Name the blood parasite species.
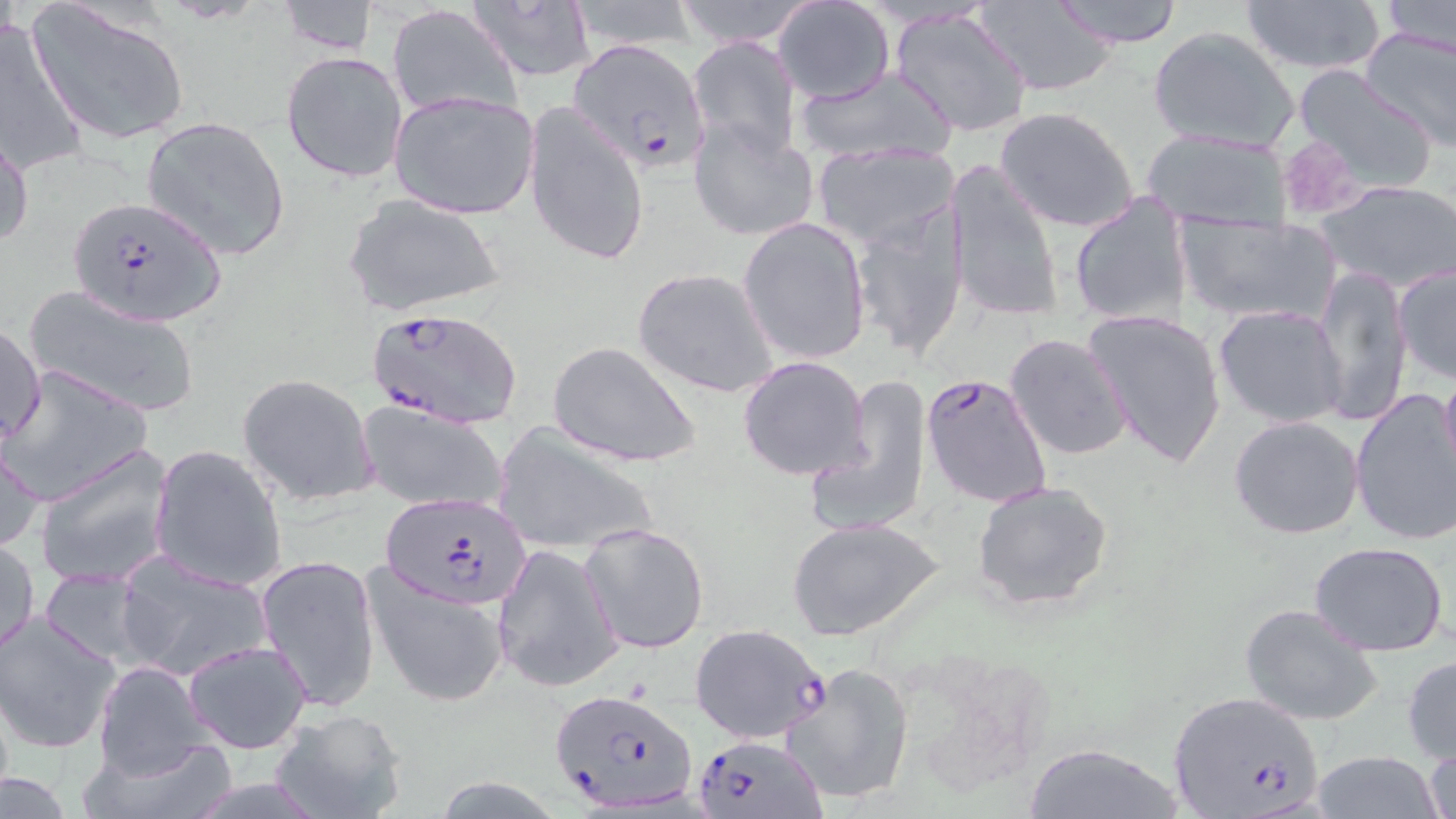

Plasmodium falciparum.

Summary:
  - Coordinate format: approximate bounding boxes as (x1, y1, x2, y2) in pixels
  - Uninfected red blood cell locations: (563, 0, 703, 53), (670, 0, 820, 48), (1048, 0, 1187, 47), (1241, 0, 1388, 75), (1380, 0, 1456, 58), (27, 1, 192, 146), (277, 1, 378, 56), (464, 2, 598, 82), (773, 2, 895, 102), (975, 2, 1120, 95), (387, 5, 522, 121), (889, 7, 1037, 137), (0, 18, 90, 174), (1147, 25, 1298, 154), (1358, 27, 1456, 152), (686, 34, 802, 166), (281, 51, 407, 184), (1293, 64, 1437, 190), (794, 65, 959, 165), (389, 88, 540, 222), (523, 99, 649, 269), (995, 106, 1140, 234), (142, 116, 291, 261), (689, 118, 819, 243), (0, 122, 33, 256), (1141, 128, 1293, 233), (812, 141, 961, 254), (943, 159, 1063, 324), (1316, 179, 1456, 292), (1068, 191, 1193, 327), (343, 193, 505, 318), (850, 205, 970, 361), (1176, 213, 1340, 325), (738, 216, 872, 364), (1393, 263, 1456, 384), (1313, 264, 1411, 427), (631, 267, 779, 398), (23, 284, 200, 418), (1213, 305, 1350, 428), (1084, 308, 1228, 469), (1, 320, 45, 445), (1005, 333, 1130, 461), (547, 340, 703, 468), (737, 356, 874, 481), (2, 366, 154, 505), (1439, 368, 1456, 483), (237, 374, 379, 506), (807, 374, 934, 537), (1349, 393, 1456, 549), (357, 399, 511, 514), (1228, 414, 1365, 539), (494, 423, 662, 556), (0, 436, 46, 556), (149, 445, 287, 591), (35, 446, 175, 589), (971, 480, 1115, 612), (787, 516, 944, 642), (579, 521, 711, 654), (2, 535, 39, 658), (1309, 540, 1450, 655), (491, 543, 622, 692), (114, 554, 273, 682), (254, 554, 382, 711), (362, 565, 510, 708), (36, 568, 151, 669), (1237, 601, 1382, 727), (0, 612, 124, 754), (179, 638, 314, 753), (1403, 654, 1456, 764), (778, 660, 917, 805), (92, 661, 217, 782), (268, 708, 409, 819), (73, 733, 240, 819), (1421, 740, 1455, 819), (1023, 741, 1182, 819), (1308, 750, 1443, 818), (0, 775, 75, 816), (432, 777, 565, 816)
  - Plasmodium falciparum-infected red blood cell locations: (567, 39, 711, 176), (65, 194, 225, 324), (365, 303, 525, 429), (922, 371, 1053, 507), (380, 492, 532, 610), (688, 623, 830, 745), (548, 687, 701, 813), (1166, 690, 1323, 819), (689, 733, 828, 818)
  - Preparation: thin blood film
  - Magnification: 1000x
  - Image size: 1456×819 pixels
  - Modality: light microscopy
  - Field of view: one of a larger specimen
  - Stain: May-Grünwald-Giemsa